Evaluate for parasitized red blood cells.
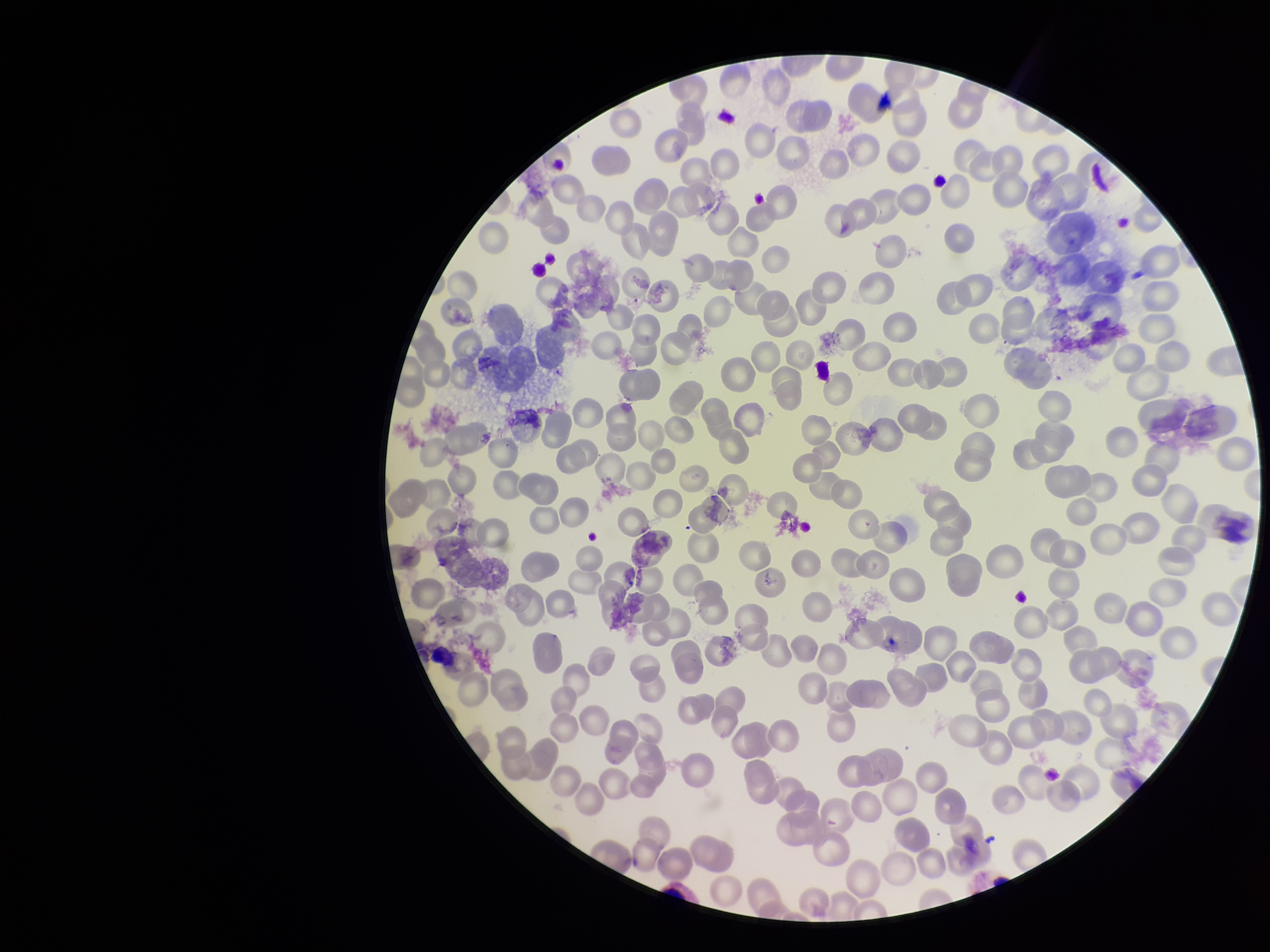

None detected.

Image is 1270×952 pixels. Parasitized red blood cell count: 0. Patient malaria status: positive. Species reported for this patient: Plasmodium vivax. Preparation: thin blood smear. One field from this slide. Red blood cell count: 229. Stained with Giemsa. Photographed through the microscope eyepiece with a smartphone camera.